Classify this cell by malaria status.
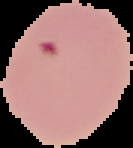
It is parasitized.

image size = 133×148 pixels
preparation = thin blood film
image type = segmented cell region on a black background